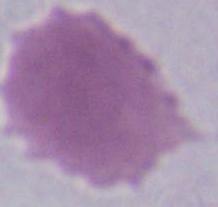 A red blood cell is shown. Photomicrograph. 1000x magnification.